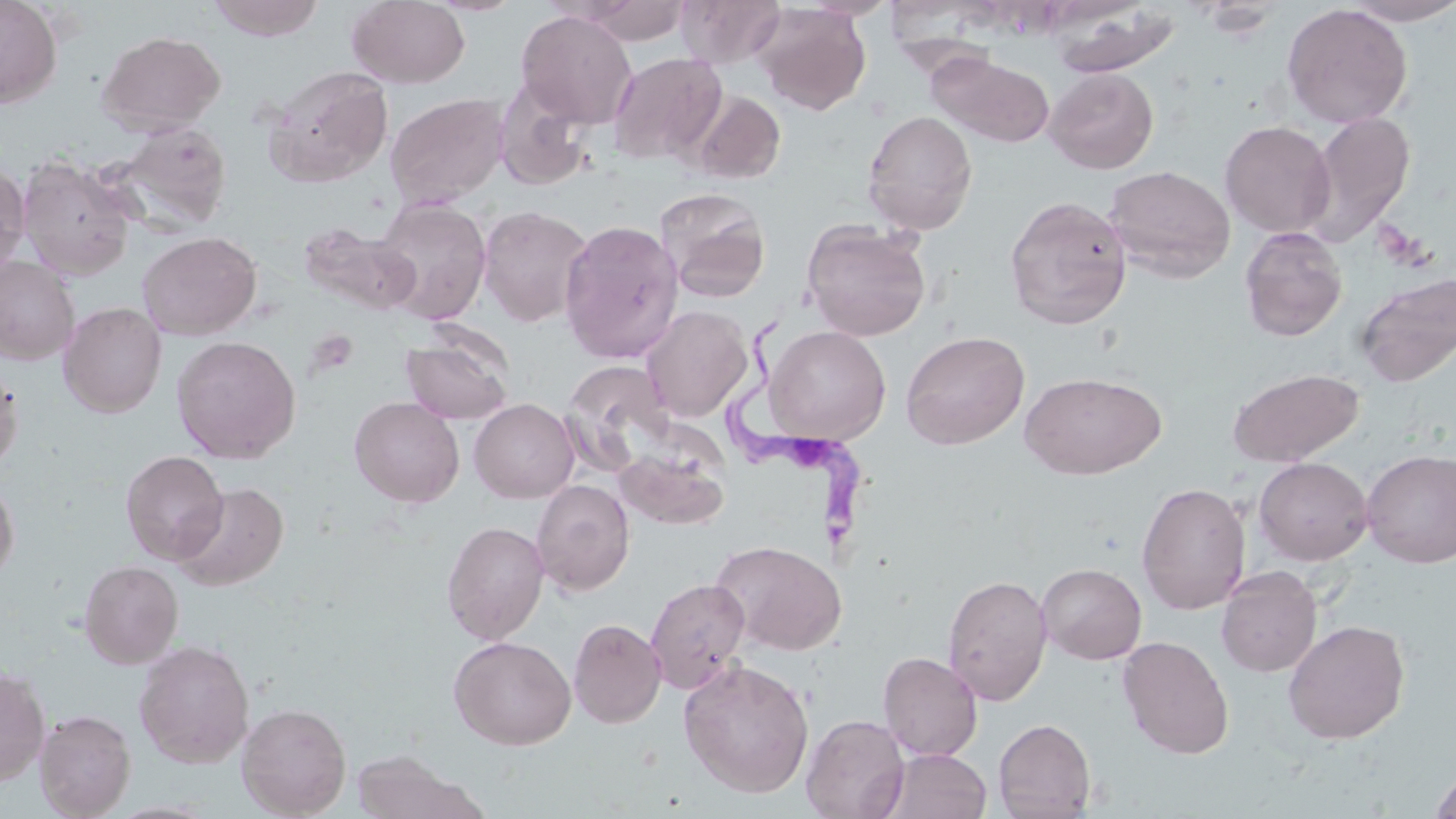
slide-level diagnosis = Trypanosoma brucei
preparation = thin blood smear
uninfected red blood cell locations = approximate bounding boxes as (x1,y1)-(x2,y2) corner pairs in pixels: (0,0)-(62,109), (207,0)-(328,42), (423,0)-(526,16), (575,0)-(693,45), (675,0)-(786,68), (800,0)-(900,20), (1341,0)-(1456,26), (346,1)-(470,88), (1192,1)-(1286,39), (754,4)-(871,115), (1281,4)-(1413,128), (1053,8)-(1182,77), (516,9)-(638,128), (97,30)-(226,136), (607,52)-(726,164), (929,52)-(1055,148), (264,65)-(394,187), (1044,67)-(1159,174), (495,83)-(595,193), (688,89)-(786,184), (385,93)-(510,208), (862,110)-(978,235), (1303,110)-(1416,246), (1220,120)-(1336,237), (109,122)-(233,233), (18,155)-(139,280), (0,164)-(30,278), (1103,165)-(1236,282), (655,188)-(771,304), (1004,194)-(1132,329), (372,197)-(492,324), (478,205)-(593,327), (558,219)-(684,363), (801,220)-(931,341), (299,223)-(419,314), (1240,227)-(1347,342), (137,231)-(261,340), (0,256)-(80,365), (1355,271)-(1456,388), (59,302)-(166,417), (641,305)-(754,422), (765,325)-(891,444), (401,329)-(514,425), (900,331)-(1030,450), (171,335)-(301,464), (560,360)-(676,474), (0,362)-(23,476), (1227,368)-(1364,467), (1019,371)-(1166,480), (349,397)-(464,508), (469,398)-(579,503), (613,446)-(731,529), (1361,449)-(1456,568), (120,450)-(229,564), (1253,457)-(1373,565), (0,475)-(19,584), (531,480)-(635,596), (1136,481)-(1251,614), (173,482)-(289,591), (442,520)-(549,644), (711,539)-(845,655), (79,560)-(184,668), (1036,562)-(1147,664), (1216,566)-(1322,677), (942,573)-(1052,706), (645,577)-(751,694), (568,618)-(666,728), (1282,619)-(1410,745), (449,635)-(576,750), (1117,636)-(1234,758), (134,640)-(255,768), (878,651)-(983,761), (678,658)-(815,798), (0,666)-(50,787), (237,702)-(352,818), (34,708)-(136,819), (801,714)-(910,819), (993,717)-(1096,818), (350,749)-(482,819), (881,749)-(991,819), (1428,767)-(1456,819)
magnification = 1000x
field of view = one of a larger specimen
Trypanosoma brucei locations = approximate bounding boxes as (x1,y1)-(x2,y2) corner pairs in pixels: (724,307)-(871,558)
stain = May-Grünwald-Giemsa
image size = 1456×819 pixels
modality = optical microscopy